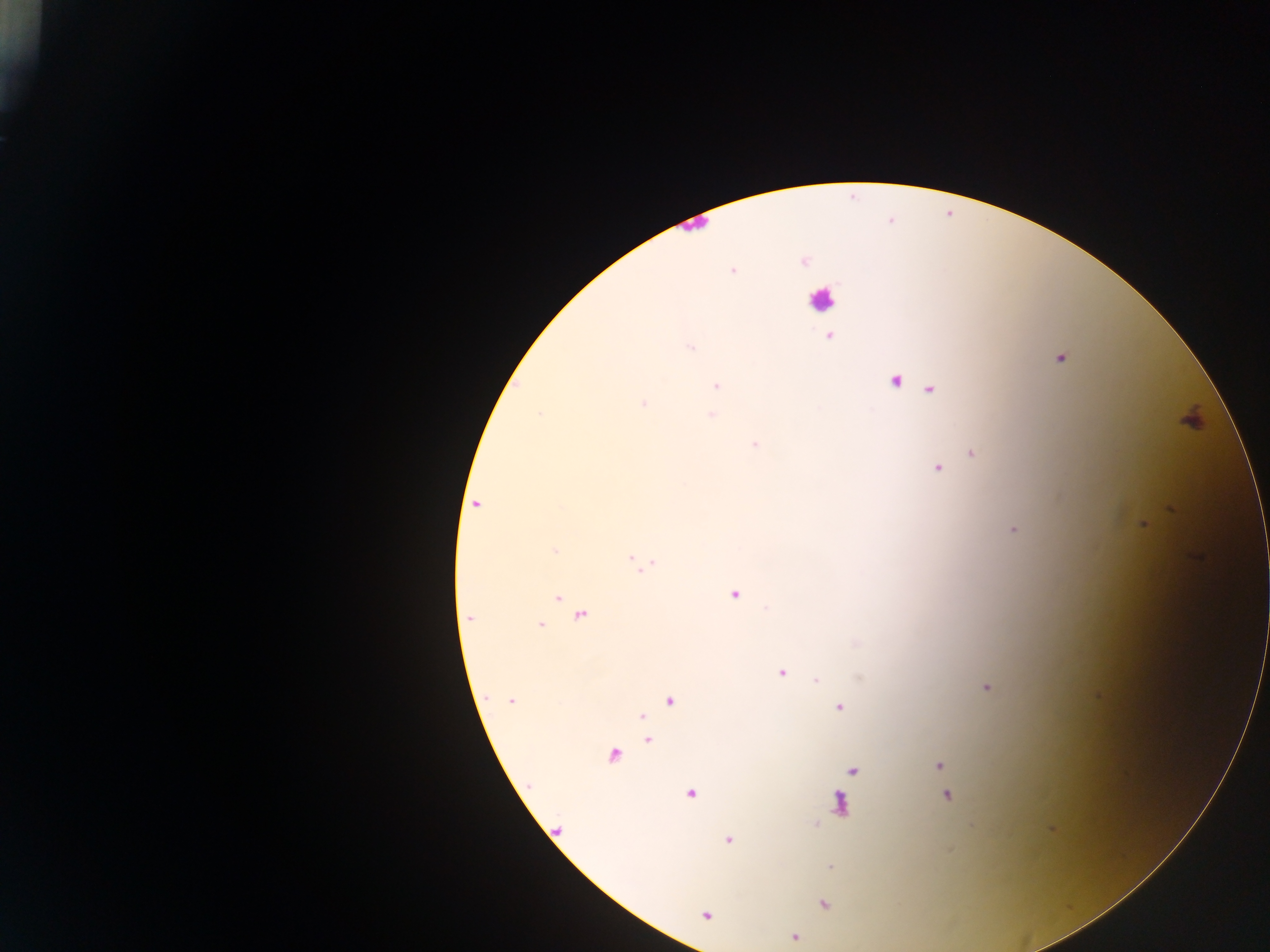
capture = mobile-phone photograph through a microscope
image size = 1270×952 pixels
leukocyte locations = approximate centers as [x, y] in pixels: [822, 300]
preparation = thick blood film
field of view = single
Plasmodium parasite locations = approximate centers as [x, y] in pixels: [804, 261], [732, 270], [829, 337], [690, 347], [1060, 358], [895, 381], [716, 386], [929, 390], [644, 404], [540, 414], [712, 416], [756, 444], [972, 454], [936, 468], [475, 504], [1143, 525], [1013, 529], [554, 550], [640, 564], [734, 595], [559, 598], [581, 616], [470, 618], [541, 625], [781, 672], [816, 680], [987, 688], [510, 700], [670, 701], [839, 708], [641, 717], [647, 740], [614, 755], [940, 766], [853, 771], [945, 783], [691, 794], [948, 795], [840, 802], [729, 840], [830, 865], [824, 904], [707, 914], [794, 937]
country = Ghana